Assess this cell for malaria.
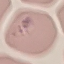
It is parasitized.

Giemsa stain. Acquired by smartphone through the microscope eyepiece. Automatically extracted cell patch, resized to 64 × 64 pixels. Thin blood smear.